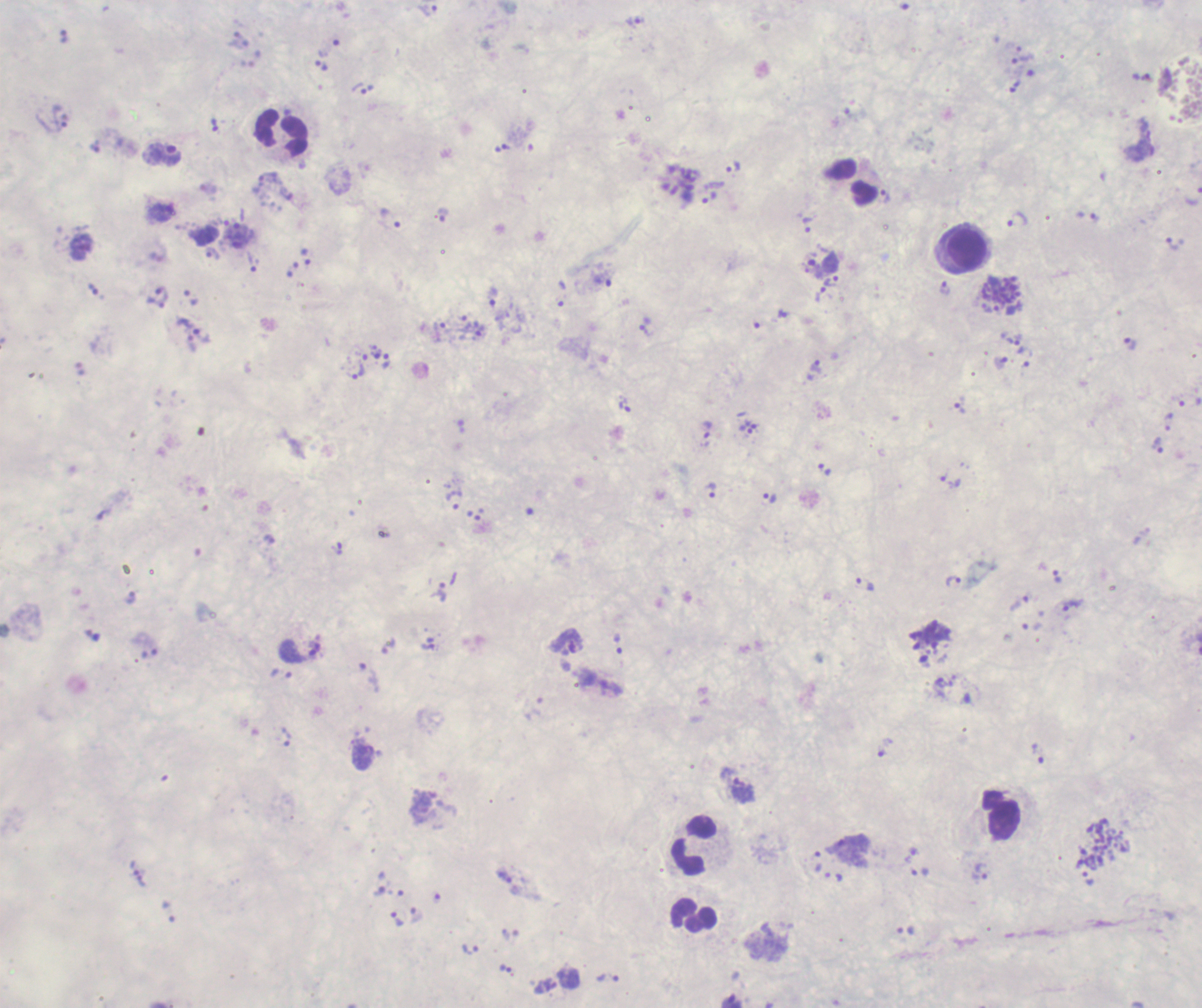
coordinate format = approximate centers as [x, y] in pixels
leukocyte locations = [282, 133], [968, 250], [1002, 815], [695, 843], [693, 915]
schizont locations = [1001, 290], [1102, 844]
trophozoite locations = [427, 10], [636, 20], [1022, 59], [322, 65], [1015, 86], [359, 89], [215, 125], [163, 155], [733, 167], [268, 178], [886, 197], [709, 198], [391, 219], [1017, 220], [807, 224], [1172, 244], [213, 254], [306, 257], [252, 263], [832, 281], [603, 282], [944, 288], [820, 294], [492, 297], [645, 326], [440, 330], [202, 336], [1015, 340], [1130, 345], [1025, 356], [386, 361], [1001, 362], [815, 366], [359, 373], [625, 405], [959, 408], [707, 430], [745, 430], [1158, 445], [951, 481], [711, 491], [769, 498], [455, 500], [337, 549], [1057, 576], [954, 581], [866, 584], [438, 591], [1019, 603], [1071, 605], [567, 642], [389, 646], [301, 651], [369, 677], [287, 737], [886, 748], [1038, 752], [742, 790], [133, 866], [980, 871], [920, 872], [505, 877], [1088, 879], [141, 881], [379, 891], [416, 915], [398, 918], [471, 949], [506, 968], [608, 978]
life-cycle stages observed = trophozoite, schizont
stain = Romanowsky
image size = 1202×1008 pixels
coloration quality = bad
background quality = unsatisfactory
preparation = thick blood smear
field of view = single
context = previously used in a real diagnosis
magnification = 100x
result = malaria parasites identified